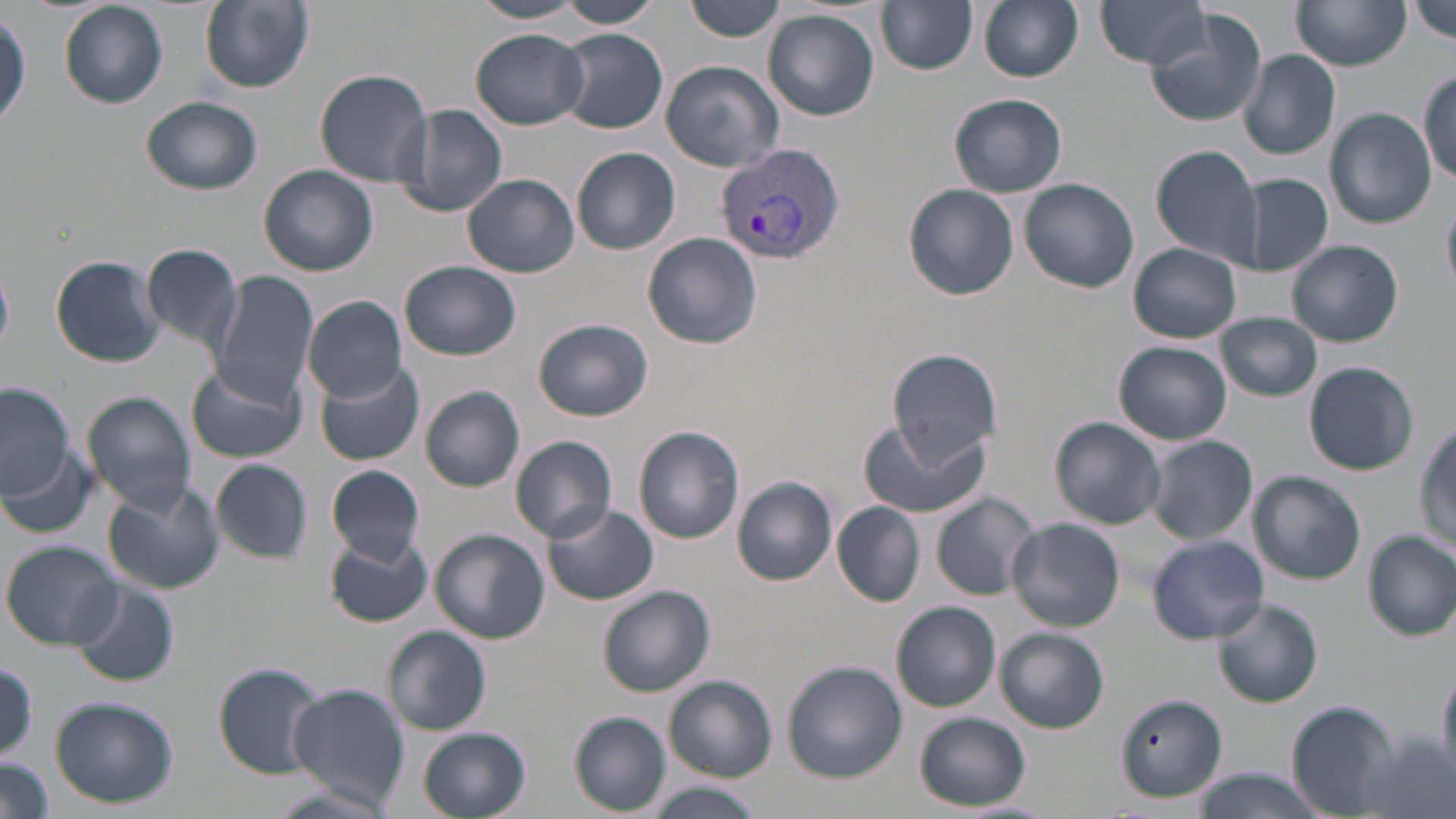

slide-level diagnosis = Plasmodium vivax
field of view = one of a larger specimen
image size = 1456×819 pixels
modality = optical microscopy
magnification = 1000x
uninfected red blood cell locations = approximate bounding boxes as (x1, y1, x2, y2) in pixels: (200, 0, 313, 95), (685, 0, 789, 44), (978, 0, 1085, 83), (467, 1, 590, 24), (557, 1, 660, 27), (877, 1, 978, 74), (1095, 1, 1213, 68), (1292, 1, 1411, 71), (1410, 1, 1455, 40), (58, 2, 168, 108), (0, 8, 30, 128), (764, 10, 879, 121), (1144, 10, 1268, 127), (471, 29, 589, 129), (555, 29, 669, 134), (1238, 50, 1340, 160), (659, 61, 785, 172), (315, 68, 437, 186), (1420, 69, 1455, 181), (949, 93, 1068, 197), (141, 96, 262, 195), (400, 105, 508, 218), (1324, 109, 1436, 228), (1151, 146, 1265, 263), (571, 147, 680, 255), (259, 164, 379, 276), (1236, 173, 1334, 276), (463, 174, 579, 277), (1020, 178, 1139, 293), (903, 182, 1018, 300), (1441, 198, 1455, 297), (643, 231, 763, 348), (1288, 239, 1402, 347), (140, 242, 245, 351), (1130, 243, 1242, 342), (50, 255, 164, 367), (402, 261, 521, 360), (209, 272, 318, 404), (304, 297, 407, 400), (1218, 312, 1322, 401), (533, 318, 653, 422), (1115, 341, 1232, 445), (888, 348, 1004, 462), (315, 359, 425, 466), (1304, 361, 1419, 475), (187, 362, 307, 464), (0, 382, 72, 499), (420, 385, 525, 492), (82, 391, 195, 513), (859, 417, 988, 520), (1050, 418, 1167, 529), (1415, 422, 1456, 553), (634, 425, 744, 543), (511, 435, 617, 544), (1143, 436, 1259, 544), (6, 446, 94, 536), (210, 459, 312, 563), (326, 463, 425, 564), (1229, 470, 1354, 676), (1248, 470, 1366, 585), (734, 477, 837, 586), (103, 482, 224, 595), (931, 491, 1040, 599), (832, 502, 926, 606), (542, 504, 659, 608), (1007, 519, 1126, 632), (430, 529, 548, 644), (324, 531, 434, 627), (1365, 531, 1455, 639), (1147, 535, 1270, 644), (3, 541, 120, 648), (69, 579, 179, 688), (597, 584, 715, 696), (892, 600, 1000, 712), (1212, 600, 1322, 707), (383, 626, 493, 736), (997, 628, 1109, 732), (0, 659, 40, 759), (783, 661, 906, 783), (213, 663, 327, 777), (1436, 664, 1456, 779), (663, 675, 776, 781), (286, 683, 409, 808), (1117, 693, 1229, 801), (49, 696, 178, 808), (1286, 701, 1400, 816), (571, 712, 670, 815), (915, 712, 1030, 810), (419, 728, 531, 819), (1, 756, 52, 819), (1187, 769, 1327, 819), (643, 784, 764, 819)
Plasmodium vivax-infected red blood cell locations = approximate bounding boxes as (x1, y1, x2, y2) in pixels: (717, 142, 845, 265)
stain = May-Grünwald-Giemsa
preparation = thin blood film